Name the cell type shown.
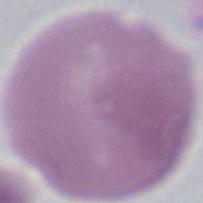
This is an erythrocyte.

Summary:
  - Modality: photomicrograph
  - Magnification: 1000x